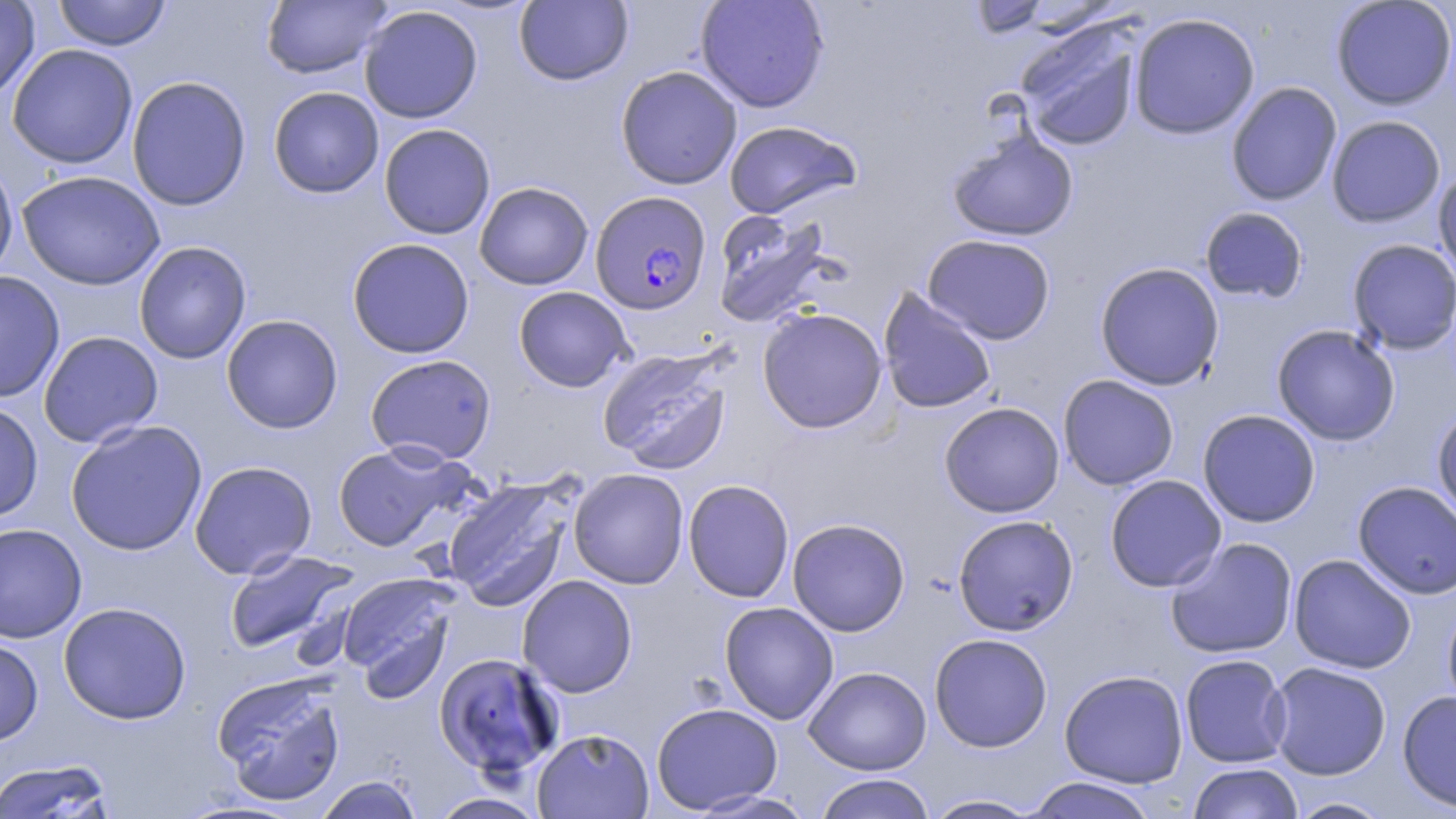

Approximate bounding boxes as (x1,y1)-(x2,y2) corner pairs in pixels. Plasmodium falciparum-infected red blood cell locations: (590,190)-(712,315). Uninfected red blood cell locations: (53,0)-(171,51), (261,0)-(391,78), (695,0)-(830,113), (969,0)-(1049,38), (1330,0)-(1456,110), (0,1)-(40,103), (514,1)-(633,85), (359,5)-(483,123), (1128,12)-(1260,139), (1014,18)-(1144,152), (7,44)-(138,169), (615,66)-(743,190), (126,75)-(252,211), (1225,82)-(1342,206), (268,86)-(384,198), (1326,115)-(1446,227), (723,120)-(862,219), (379,123)-(496,240), (946,126)-(1079,243), (0,154)-(18,284), (1433,164)-(1456,286), (16,170)-(166,291), (474,182)-(594,290), (1199,207)-(1308,304), (711,208)-(837,328), (922,233)-(1056,344), (347,238)-(475,358), (1347,239)-(1456,354), (133,241)-(251,364), (1095,262)-(1225,391), (0,271)-(65,403), (513,286)-(634,392), (877,287)-(997,415), (756,307)-(888,434), (221,314)-(343,434), (1271,324)-(1400,446), (38,331)-(163,448), (597,345)-(734,474), (365,353)-(497,466), (1058,374)-(1179,490), (0,400)-(43,523), (939,402)-(1064,518), (1432,407)-(1456,527), (1197,409)-(1321,527), (65,419)-(208,556), (333,442)-(467,552), (189,460)-(317,579), (569,468)-(689,589), (1104,474)-(1227,592), (442,477)-(575,611), (682,479)-(795,603), (1352,481)-(1456,599), (953,514)-(1078,636), (788,518)-(910,636), (0,522)-(87,643), (1165,537)-(1298,659), (225,549)-(357,655), (1288,554)-(1416,674), (336,572)-(461,699), (517,575)-(638,697), (1443,595)-(1456,718), (719,601)-(839,724), (58,602)-(192,724), (929,632)-(1053,752), (0,637)-(43,746), (434,652)-(565,778), (1179,654)-(1292,768), (1266,661)-(1392,780), (803,666)-(932,775), (1059,669)-(1188,788), (212,671)-(348,806), (1397,690)-(1456,811), (651,702)-(783,813), (532,728)-(654,818), (0,759)-(118,818), (1187,762)-(1303,819), (813,773)-(937,819), (315,775)-(423,819), (1021,777)-(1160,818), (686,788)-(816,818), (428,791)-(550,818), (922,793)-(1043,818), (1287,797)-(1394,818). Slide-level diagnosis: Plasmodium falciparum. Image is 1456×819 pixels. May-Grünwald-Giemsa stain. Single field of view. Thin blood smear. Light microscopy. 1000x magnification.